Locate Plasmodium parasites and leukocytes.
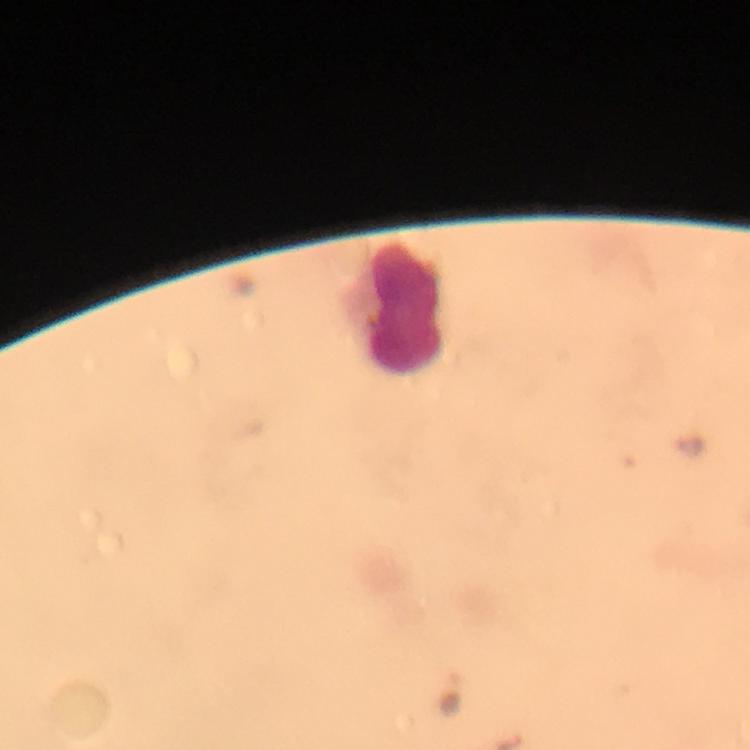
Approximate centers as (x, y) in pixels.
Plasmodium parasites: (690, 444).
Leukocytes: (404, 309).

Summary:
  - Immersion oil: used
  - Capture: smartphone photograph through a microscope
  - Image size: 750×750 pixels
  - Preparation: thick smear
  - Context: from a diagnostic examination for malaria
  - Magnification: 100x
  - Stain: Giemsa
  - Cropped from: one field of view